Identify the parasite.
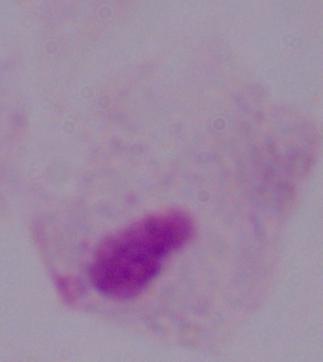
This is a trichomonad.

Summary:
  - Modality: photomicrograph
  - Magnification: 1000x